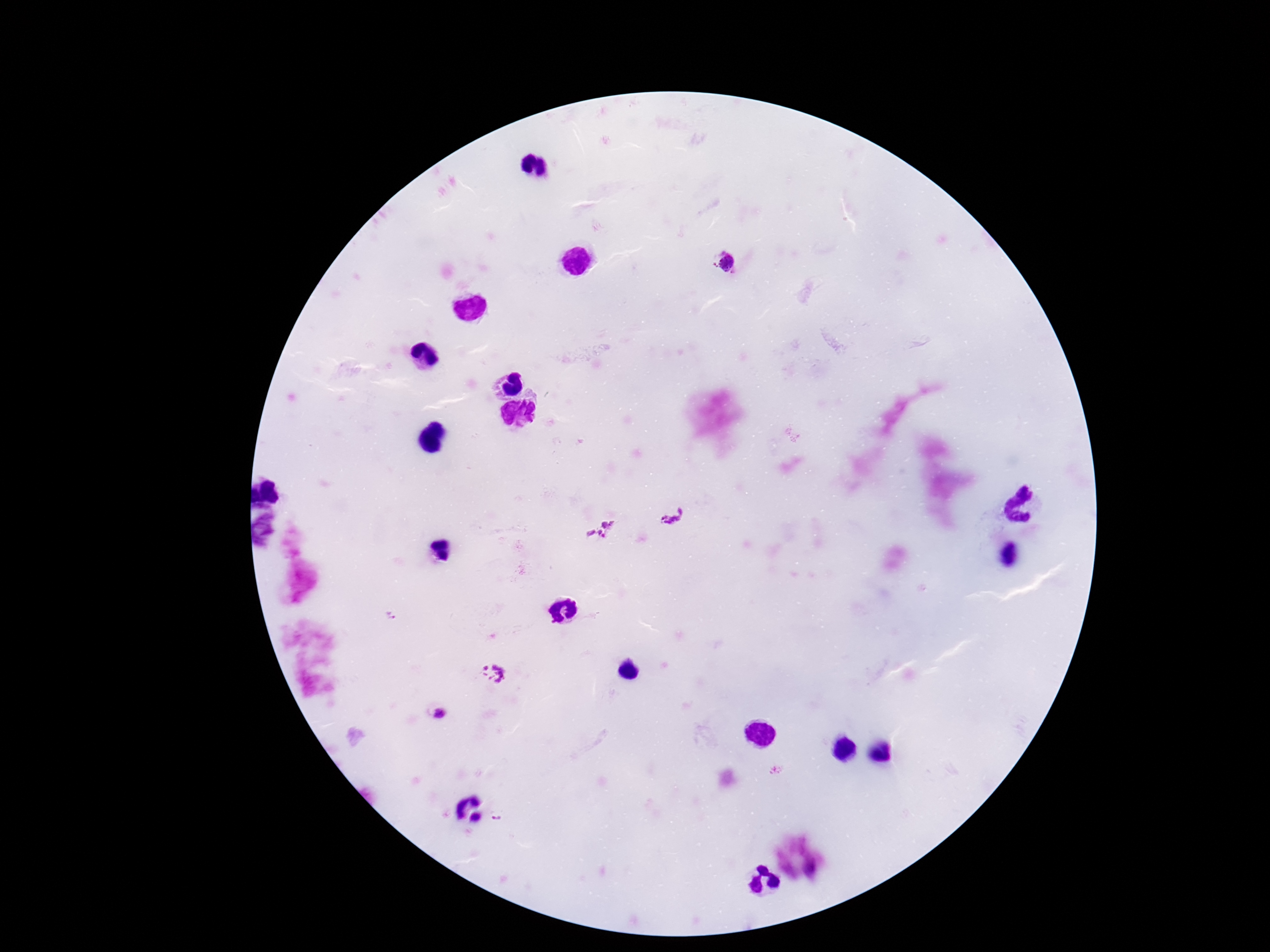

Approximate centers as (x, y) in pixels.
Summary:
  - Plasmodium parasite locations: (727, 260), (672, 513), (602, 528), (393, 616), (493, 673), (436, 714), (501, 820)
  - Stain: Giemsa
  - Magnification: 100x
  - Field of view: single
  - Patient malaria status: positive
  - Preparation: thick peripheral-blood smear
  - Image size: 1270×952 pixels
  - Capture: smartphone camera through the microscope eyepiece